Assess this cell for malaria.
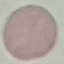

Uninfected.

Cell patch, automatically extracted from a larger field of view and resized to 64 × 64 pixels. Giemsa-stained preparation. Photographed with a smartphone camera at the microscope eyepiece. Thin smear of blood.